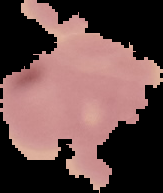

Summary:
  - Image size: 163×193 pixels
  - Result: no Plasmodium parasites detected
  - Image type: segmented cell region on a black background
  - Preparation: thin blood film